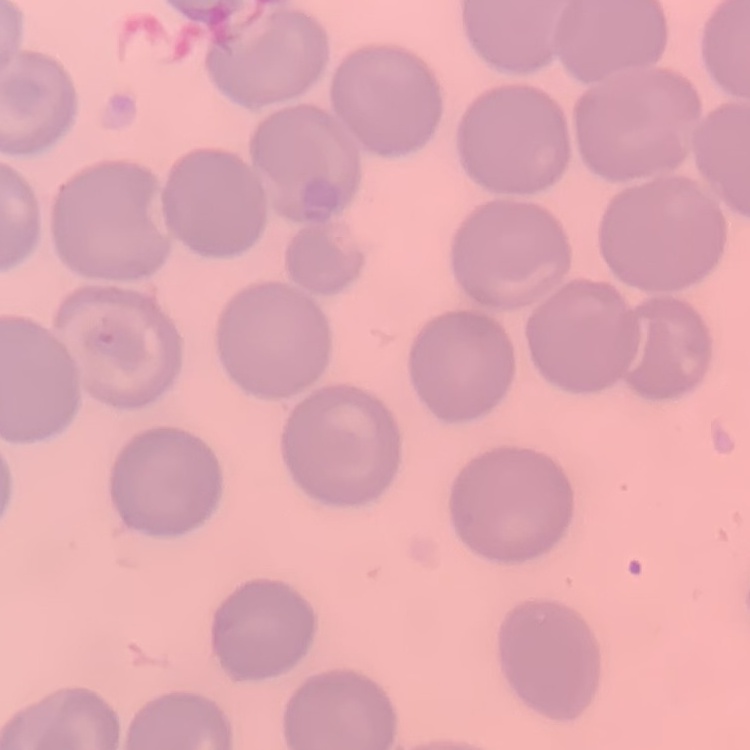

erythrocyte morphology = no rouleaux formation
preparation = thin blood film
stain = Field's or Giemsa
image type = square crop of a larger photomicrograph